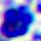
Summary:
  - Magnification: 400x
  - Modality: micrograph
  - Identification: white blood cell